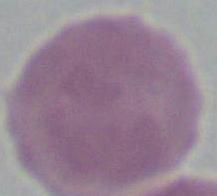
magnification = 1000x
modality = micrograph
identification = red blood cell